Comment on the morphology of the erythrocytes.
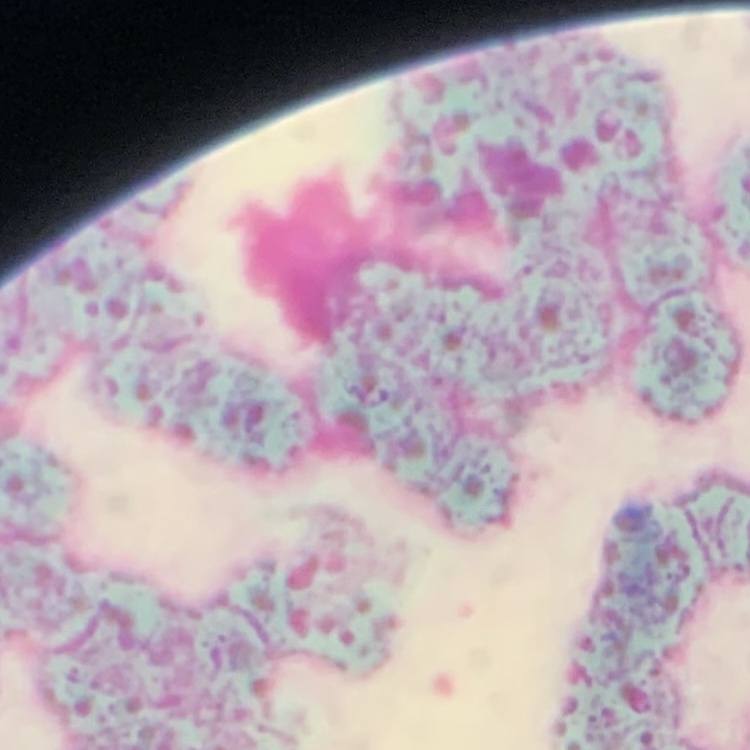

They show rouleaux formation.

stain: Field's or Giemsa
image_type: one tile cut from a larger photomicrograph
preparation: thin blood smear